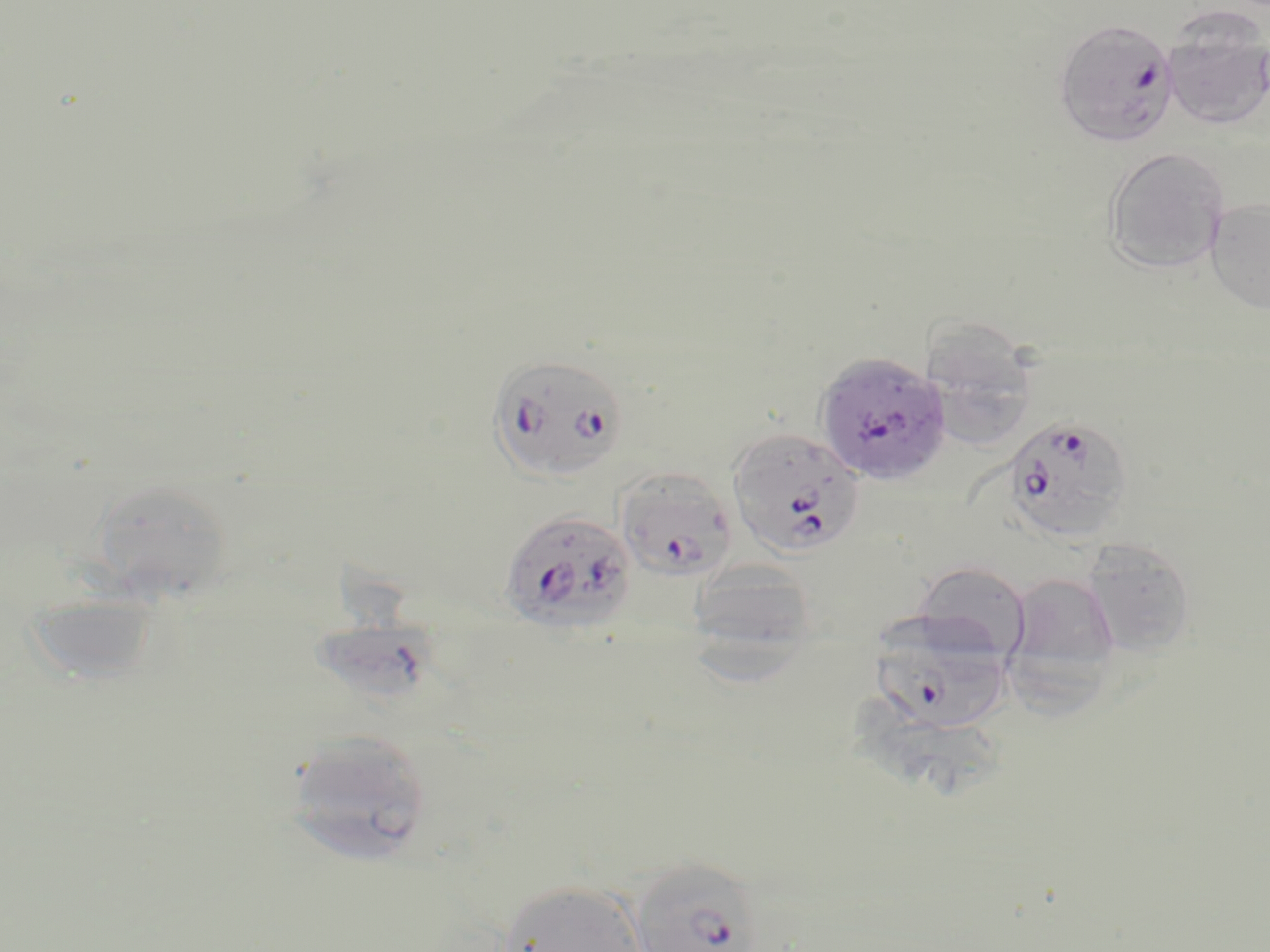
slide-level diagnosis = Plasmodium falciparum
uninfected red blood cell locations = approximate bounding boxes as (x1,y1)-(x2,y2) corner pairs in pixels: (1162,23)-(1270,130), (1103,146)-(1231,274), (1205,197)-(1270,314), (919,320)-(1042,450), (65,476)-(229,611), (1080,538)-(1198,657), (686,557)-(822,664), (911,561)-(1031,663), (1006,571)-(1121,687), (24,591)-(161,687), (283,730)-(433,864), (496,878)-(647,952)
stain = May-Grünwald-Giemsa
field of view = single
magnification = 1000x
Plasmodium falciparum-infected red blood cell locations = approximate bounding boxes as (x1,y1)-(x2,y2) corner pairs in pixels: (1054,18)-(1179,147), (814,351)-(953,486), (488,356)-(630,486), (1002,414)-(1136,543), (728,428)-(866,558), (615,468)-(737,582), (498,509)-(637,636), (870,619)-(1010,735), (629,856)-(765,952)
modality = light microscopy
image size = 1270×952 pixels
preparation = thin blood film